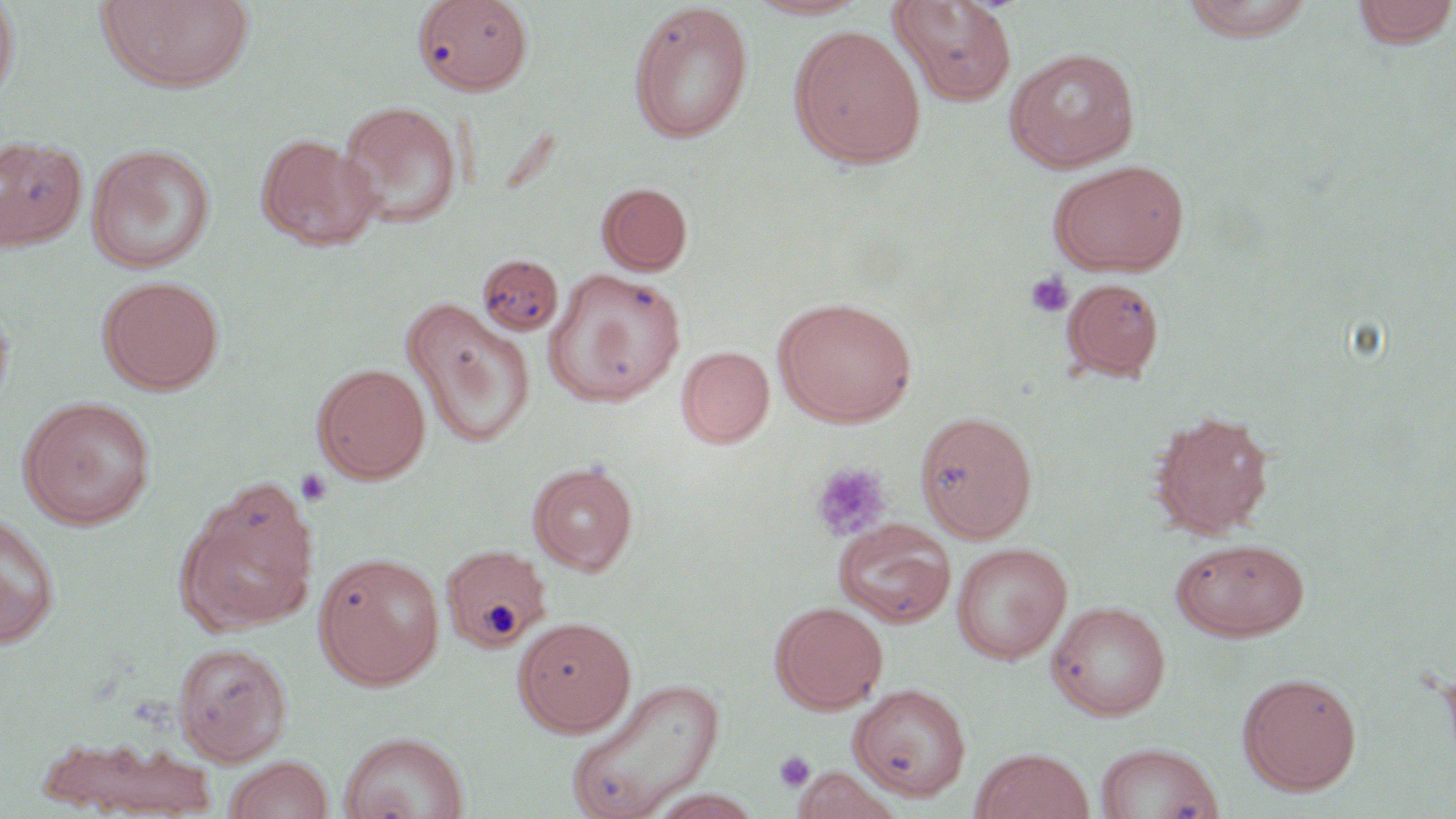
slide_level_diagnosis: negative for blood parasites
preparation: thin blood film
image_size: 1456×819 pixels
modality: light microscopy
platelet_locations: 'approximate bounding boxes as (x1, y1, x2, y2) in pixels: (1023, 271, 1074, 318), (811, 462, 892, 541), (295, 468, 333, 508), (775, 750, 816, 791)'
uninfected_red_blood_cell_locations: 'approximate bounding boxes as (x1, y1, x2, y2) in pixels: (95, 0, 257, 93), (413, 0, 535, 96), (744, 0, 871, 20), (888, 0, 1018, 106), (1181, 0, 1317, 43), (1351, 0, 1456, 48), (0, 2, 20, 104), (627, 3, 755, 144), (789, 25, 926, 168), (1003, 47, 1140, 172), (336, 100, 463, 229), (256, 133, 379, 250), (0, 136, 88, 253), (86, 143, 216, 274), (1048, 159, 1191, 277), (597, 182, 693, 275), (476, 254, 564, 337), (544, 267, 687, 407), (98, 276, 225, 394), (1061, 277, 1166, 382), (0, 294, 15, 411), (401, 297, 536, 448), (775, 297, 916, 427), (677, 346, 775, 448), (312, 363, 431, 483), (18, 396, 157, 529), (916, 410, 1037, 543), (1149, 410, 1275, 539), (529, 461, 637, 576), (176, 498, 315, 635), (0, 512, 61, 647), (833, 518, 956, 628), (1171, 537, 1311, 641), (952, 542, 1072, 664), (441, 544, 552, 652), (314, 551, 445, 689), (1048, 600, 1171, 720), (771, 601, 888, 713), (513, 616, 637, 736), (173, 642, 292, 764), (1238, 671, 1362, 795), (564, 676, 725, 819), (848, 683, 971, 802), (339, 731, 470, 819), (35, 732, 220, 816), (1095, 741, 1224, 818), (970, 748, 1094, 819), (221, 756, 334, 819), (790, 765, 904, 819)'
stain: May-Grünwald-Giemsa
field_of_view: one of a larger specimen
magnification: 1000x